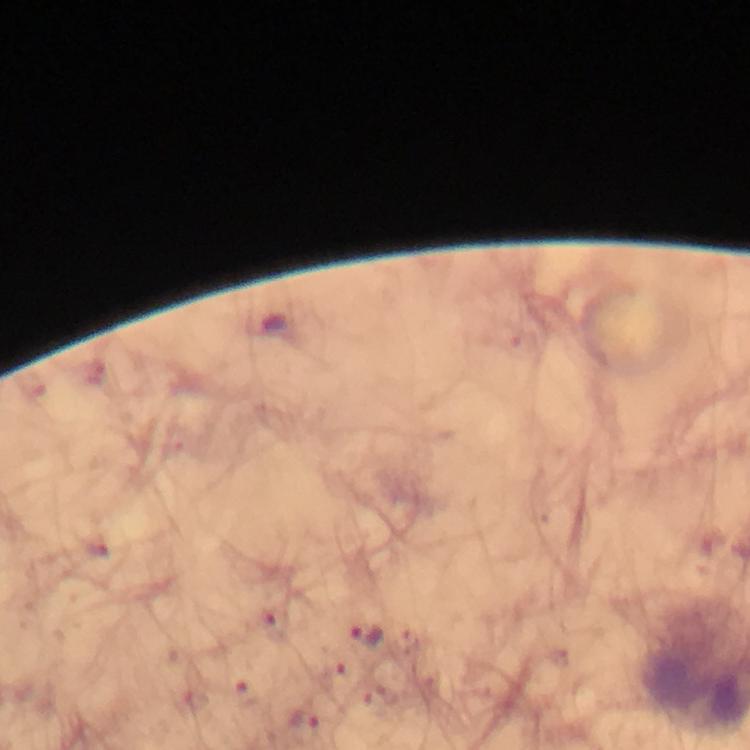
Approximate centers as [x, y] in pixels.
Summary:
  - Plasmodium parasite locations: [365, 635]
  - Capture: smartphone camera through the microscope
  - Context: from a diagnostic examination for malaria
  - Immersion oil: applied
  - Cropped from: one field of view
  - Magnification: 100x
  - Stain: Giemsa
  - Preparation: thick blood smear
  - Image size: 750×750 pixels